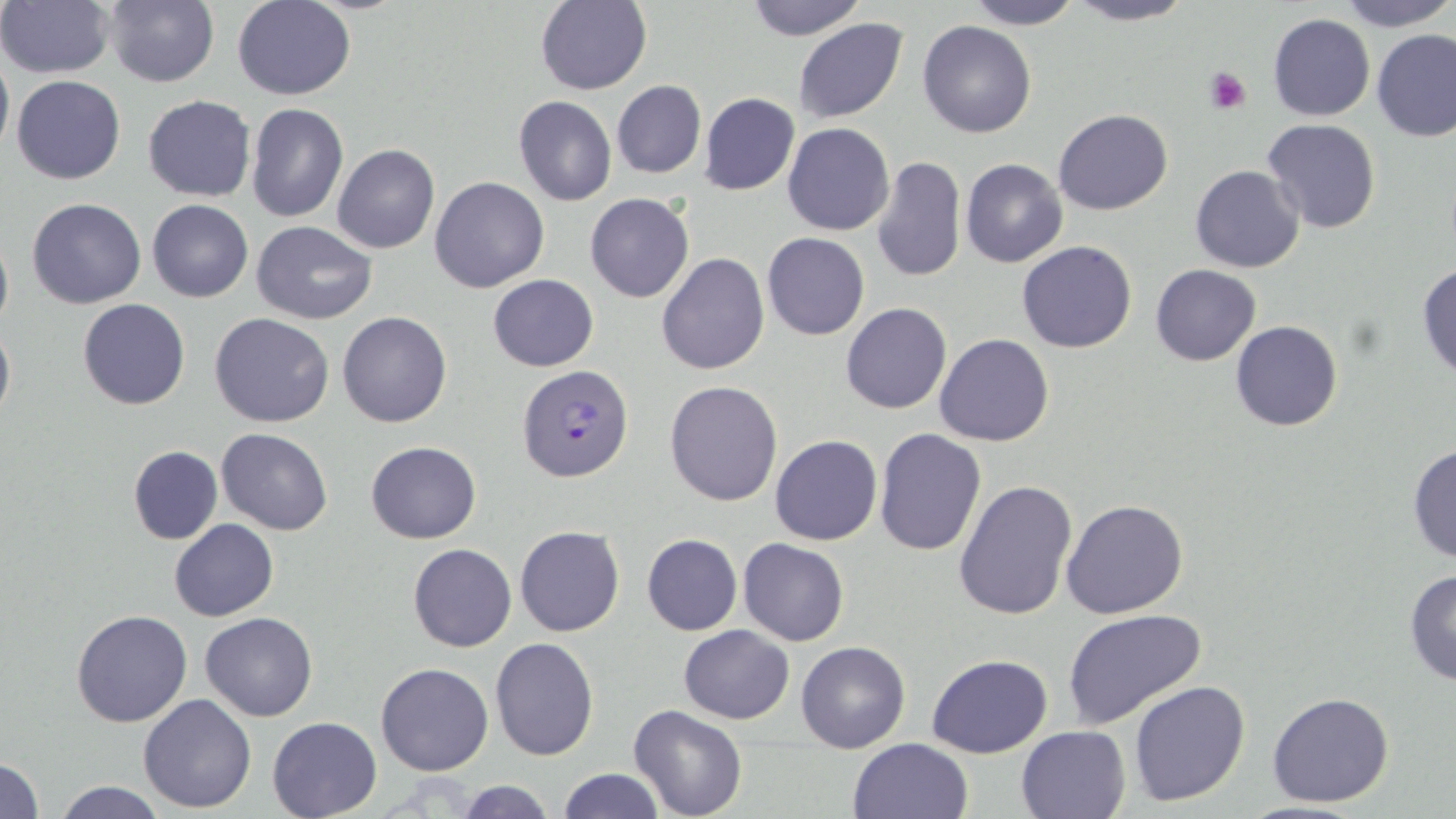
slide-level diagnosis = Plasmodium falciparum
magnification = 1000x
preparation = thin blood smear
field of view = single
platelet locations = approximate bounding boxes as (x1, y1, x2, y2) in pixels: (1204, 67, 1252, 114)
uninfected red blood cell locations = approximate bounding boxes as (x1, y1, x2, y2) in pixels: (233, 0, 355, 100), (744, 0, 868, 40), (965, 0, 1084, 29), (1067, 0, 1195, 26), (1334, 0, 1456, 31), (99, 1, 219, 87), (535, 1, 653, 95), (1, 2, 114, 79), (1268, 14, 1375, 121), (794, 18, 908, 124), (918, 19, 1036, 139), (1373, 31, 1456, 143), (0, 45, 13, 159), (12, 76, 125, 185), (613, 81, 705, 178), (699, 92, 800, 195), (142, 95, 256, 201), (513, 96, 617, 206), (246, 102, 348, 223), (1053, 109, 1173, 215), (1262, 119, 1383, 236), (783, 123, 895, 236), (332, 143, 440, 254), (872, 156, 966, 284), (961, 159, 1068, 268), (1190, 164, 1306, 273), (429, 176, 550, 293), (585, 192, 694, 304), (28, 198, 145, 308), (147, 199, 253, 301), (253, 221, 377, 324), (0, 229, 12, 338), (762, 232, 870, 340), (1017, 240, 1137, 353), (658, 253, 769, 376), (1416, 260, 1456, 382), (1150, 263, 1260, 365), (487, 275, 599, 371), (77, 298, 190, 411), (840, 303, 951, 415), (337, 310, 452, 428), (209, 313, 333, 427), (0, 320, 14, 425), (1231, 320, 1343, 432), (934, 333, 1055, 446), (665, 380, 782, 505), (215, 428, 333, 534), (873, 428, 988, 556), (770, 434, 882, 546), (365, 441, 481, 544), (1407, 443, 1456, 564), (127, 446, 222, 544), (953, 479, 1077, 622), (1061, 497, 1190, 620), (169, 520, 278, 621), (514, 526, 625, 637), (642, 534, 743, 636), (738, 538, 849, 646), (407, 543, 517, 652), (1403, 568, 1456, 690), (71, 609, 191, 728), (1063, 609, 1209, 730), (201, 612, 317, 722), (678, 624, 794, 723), (490, 637, 601, 761), (795, 641, 910, 752), (927, 654, 1054, 758), (376, 662, 494, 777), (1127, 680, 1251, 806), (1266, 691, 1395, 809), (138, 693, 257, 814), (628, 705, 746, 819), (266, 716, 380, 819), (1015, 725, 1132, 819), (847, 737, 974, 819), (0, 756, 43, 817), (558, 768, 665, 818), (453, 779, 555, 818), (52, 780, 169, 818)
image size = 1456×819 pixels
modality = optical microscopy
Plasmodium falciparum-infected red blood cell locations = approximate bounding boxes as (x1, y1, x2, y2) in pixels: (516, 365, 634, 483)
stain = May-Grünwald-Giemsa